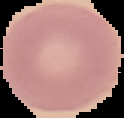
image type = cell region segmented out of the field of view; surrounding area masked to black
preparation = thin blood smear
image size = 124×118 pixels
result = negative for Plasmodium parasites